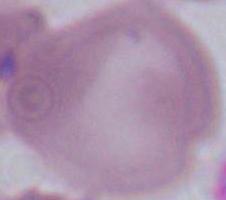

modality = photomicrograph
magnification = 1000x
identification = red blood cell